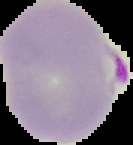
Summary:
  - Preparation: thin blood smear
  - Image size: 133×145 pixels
  - Image type: cell region segmented out of the field of view; surrounding area masked to black
  - Result: malaria parasites detected